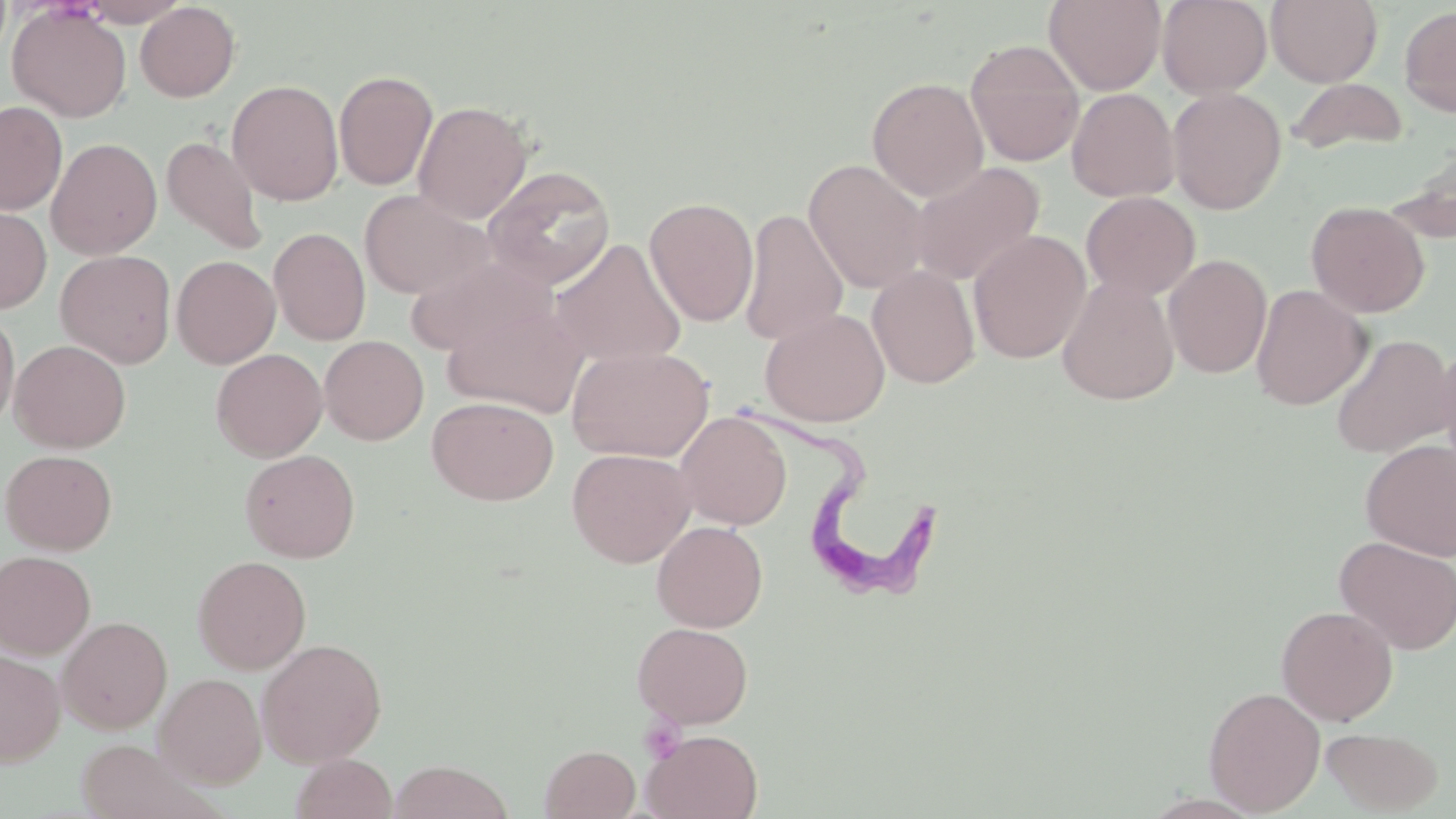
Approximate bounding boxes as (x1,y1)-(x2,y2) corner pairs in pixels. Trypanosoma brucei locations: (740,395)-(942,599). Uninfected red blood cell locations: (78,0)-(190,27), (1044,0)-(1166,95), (1157,0)-(1272,99), (1266,0)-(1382,87), (135,2)-(240,102), (7,4)-(131,122), (1399,6)-(1456,118), (964,39)-(1086,167), (333,69)-(438,191), (867,76)-(989,201), (1287,78)-(1409,156), (227,79)-(343,205), (1167,87)-(1287,214), (1066,88)-(1180,202), (413,100)-(533,224), (0,101)-(67,215), (161,135)-(268,256), (46,137)-(162,260), (1393,144)-(1456,241), (804,159)-(930,294), (908,161)-(1045,286), (482,165)-(617,289), (358,189)-(494,300), (1081,191)-(1200,300), (644,196)-(759,327), (1306,200)-(1430,318), (0,204)-(52,314), (739,208)-(849,347), (269,227)-(370,345), (968,230)-(1092,364), (550,238)-(688,367), (56,250)-(177,368), (1163,253)-(1272,379), (406,254)-(556,358), (171,255)-(280,368), (867,265)-(980,388), (1057,276)-(1180,405), (1250,284)-(1372,410), (442,300)-(590,418), (759,307)-(890,426), (0,308)-(19,433), (1330,334)-(1455,459), (319,335)-(429,445), (9,340)-(131,452), (1432,343)-(1456,477), (567,345)-(714,463), (211,348)-(328,461), (426,396)-(559,505), (675,411)-(792,530), (1360,440)-(1456,561), (566,447)-(696,567), (1,449)-(118,555), (240,449)-(360,563), (651,520)-(768,632), (1335,536)-(1456,654), (0,550)-(95,658), (192,554)-(311,674), (1276,605)-(1398,725), (57,616)-(172,734), (632,621)-(753,729), (256,638)-(387,767), (0,648)-(65,766), (154,672)-(266,788), (1203,686)-(1326,815), (1321,726)-(1443,814), (642,729)-(763,818), (74,738)-(217,819), (539,745)-(640,819), (291,753)-(397,819), (388,760)-(514,819). Slide-level diagnosis: Trypanosoma brucei. May-Grünwald-Giemsa stain. 1000x magnification. Optical microscopy. Single field of view. Thin blood film. Image is 1456×819 pixels.